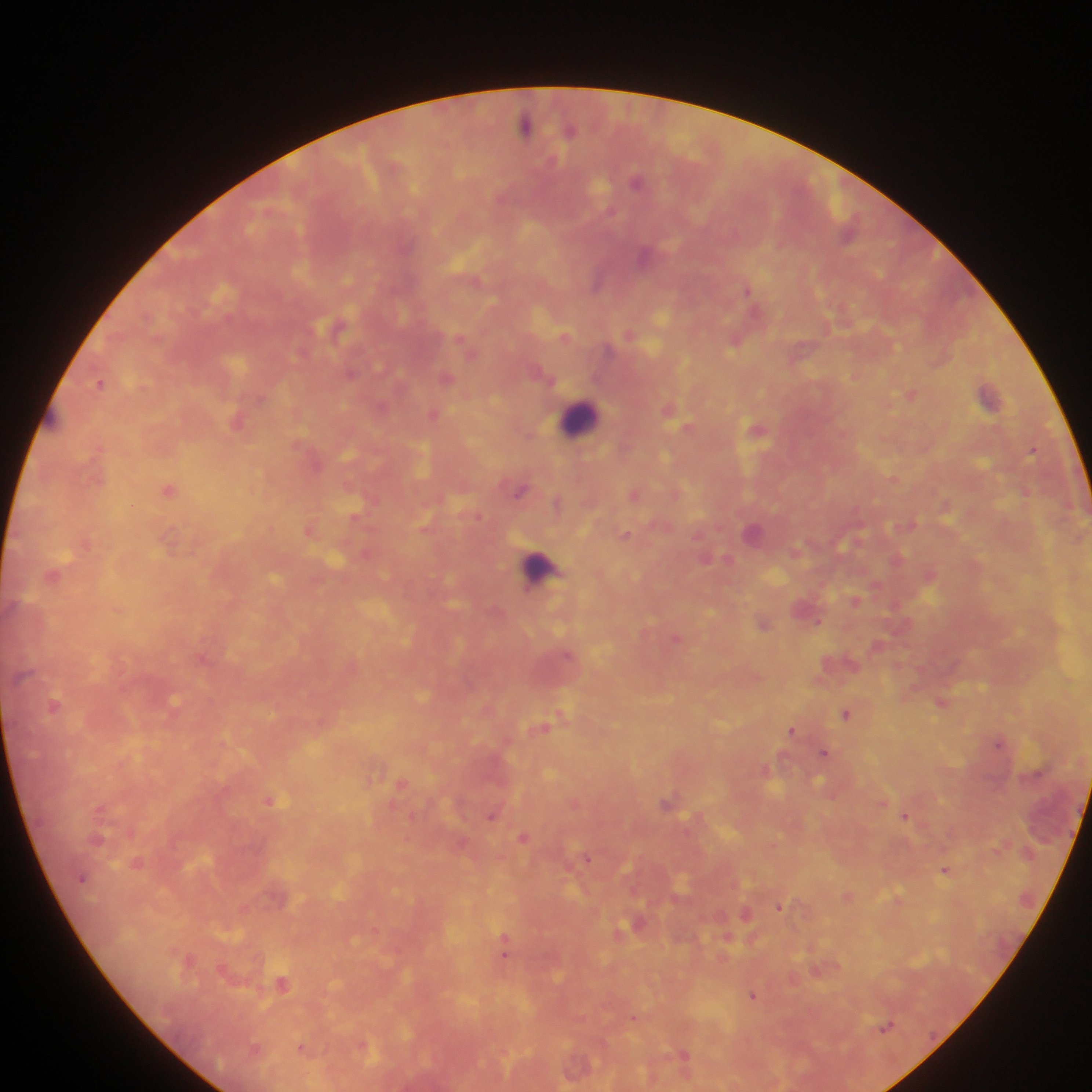
Approximate centers as x y in pixels. Plasmodium parasite locations: 525 125; 571 131; 636 181; 643 256; 597 282; 748 289; 734 343; 446 377; 100 382; 911 394; 988 395; 434 414; 236 423; 757 430; 1032 451; 169 490; 520 491; 478 517; 626 534; 854 600; 819 622; 763 623; 676 638; 567 654; 940 703; 54 706; 845 714; 791 730; 998 743; 824 753; 271 802; 667 802; 491 815; 906 816; 524 836; 587 857; 945 870; 779 907; 504 947; 188 959; 282 983; 752 995; 886 1026; 301 1048; 684 1055. Leukocyte locations: 580 417; 541 569. One field of view. Photographed through a microscope with a mobile-phone camera. Thick blood smear. Image is 1092×1092 pixels. Collected in Ghana.